Give the position of every malaria parasite.
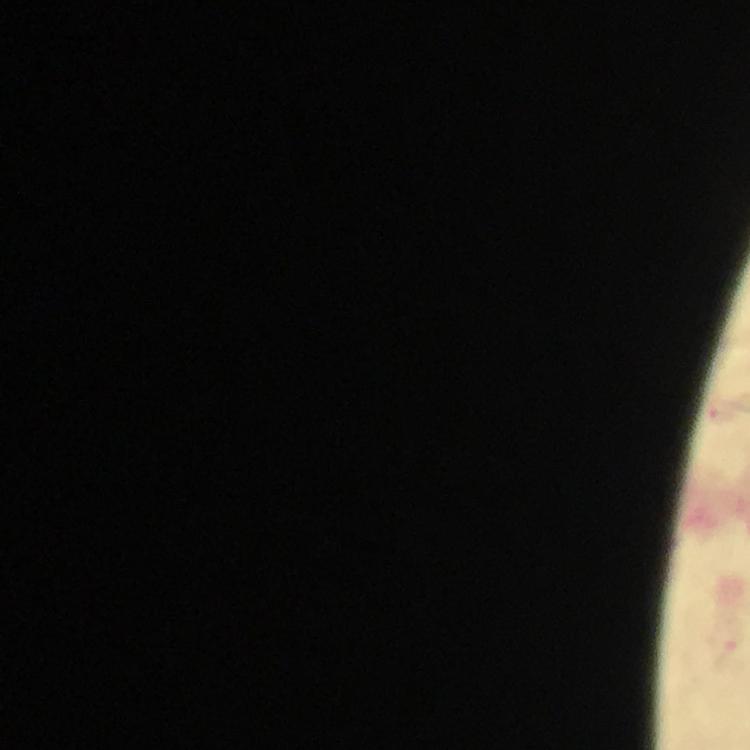
Approximate centers as [x, y] in pixels.
Malaria parasites: [722, 414], [729, 643].

Summary:
  - Context: from a diagnostic examination for malaria
  - Immersion oil: applied
  - Capture: smartphone mounted on the microscope
  - Image size: 750×750 pixels
  - Stain: Giemsa
  - Magnification: 100x
  - Preparation: thick smear
  - Cropped from: one field of view